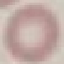

result: negative for malaria parasites
stain: Giemsa
capture: smartphone through the microscope eyepiece
image_type: cell patch, automatically extracted from a larger field of view and resized to 64 × 64 pixels
preparation: thin blood film